Locate every Plasmodium parasite.
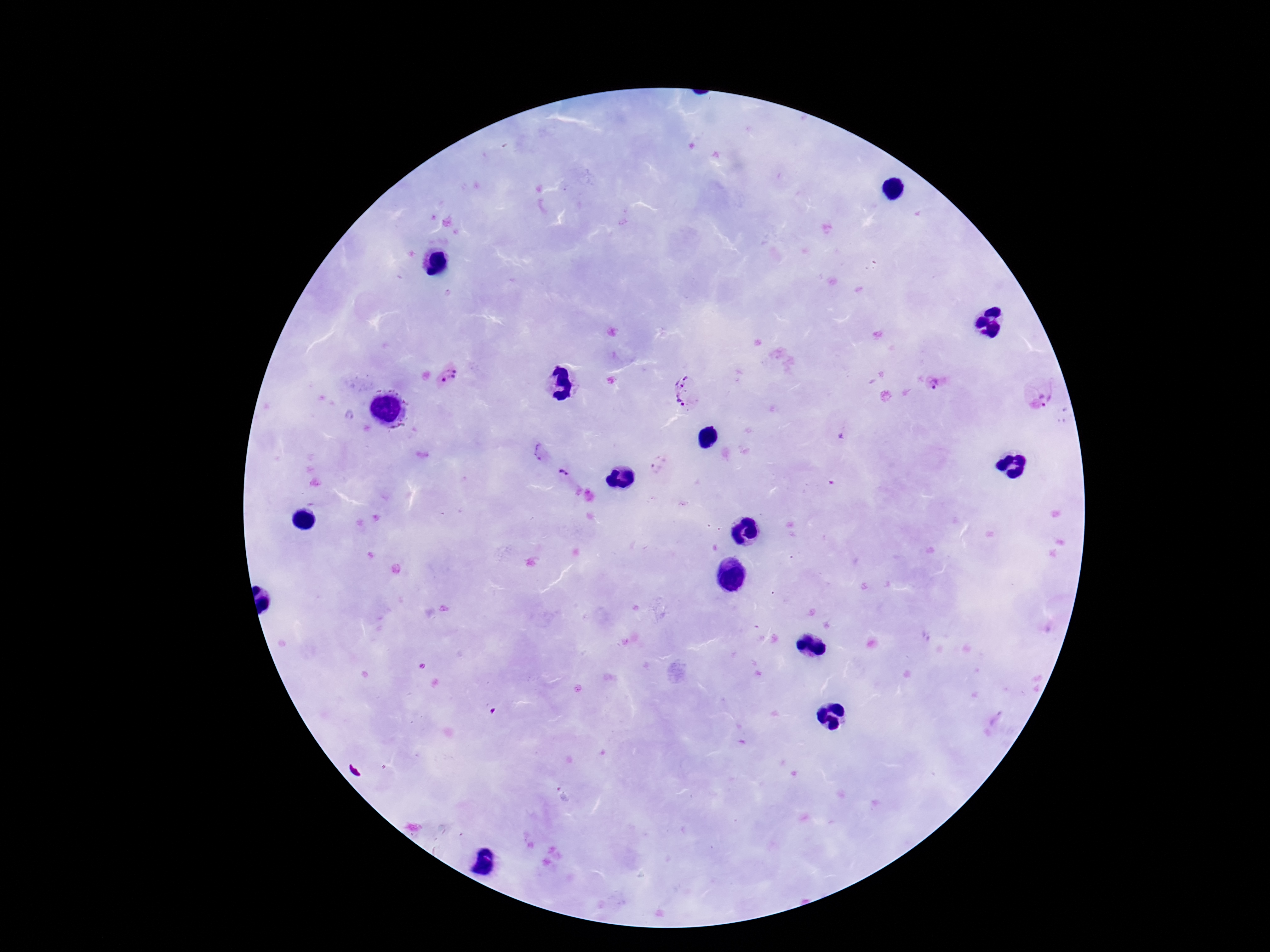

Approximate centers as (x, y) in pixels.
Plasmodium parasites: (449, 378), (934, 384), (1050, 393), (690, 394), (841, 434), (542, 453), (659, 465), (563, 475).

Summary:
  - Patient malaria status: infected
  - Field of view: one from this slide
  - Image size: 1270×952 pixels
  - Magnification: 100x
  - Preparation: thick blood film
  - Stain: Giemsa
  - Capture: smartphone camera through the microscope eyepiece